Report the malaria status of this cell.
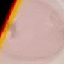

Uninfected.

image type = automatically extracted cell patch, resized to 64 × 64 pixels
preparation = thin blood smear
stain = Giemsa
capture = smartphone camera at the microscope eyepiece